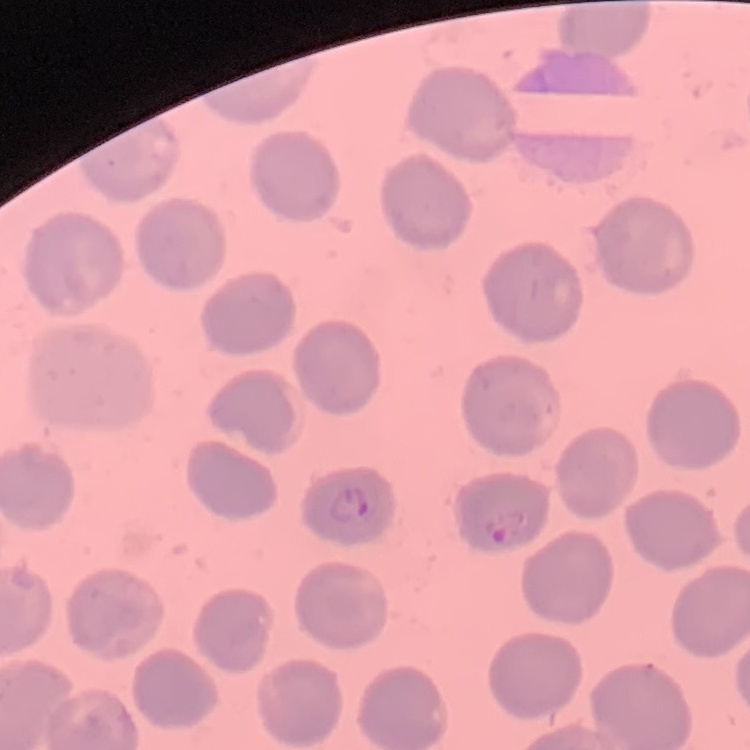

red_blood_cell_morphology: no rouleaux formation
stain: Field's or Giemsa
preparation: thin blood film
image_type: one tile cut from a larger photomicrograph